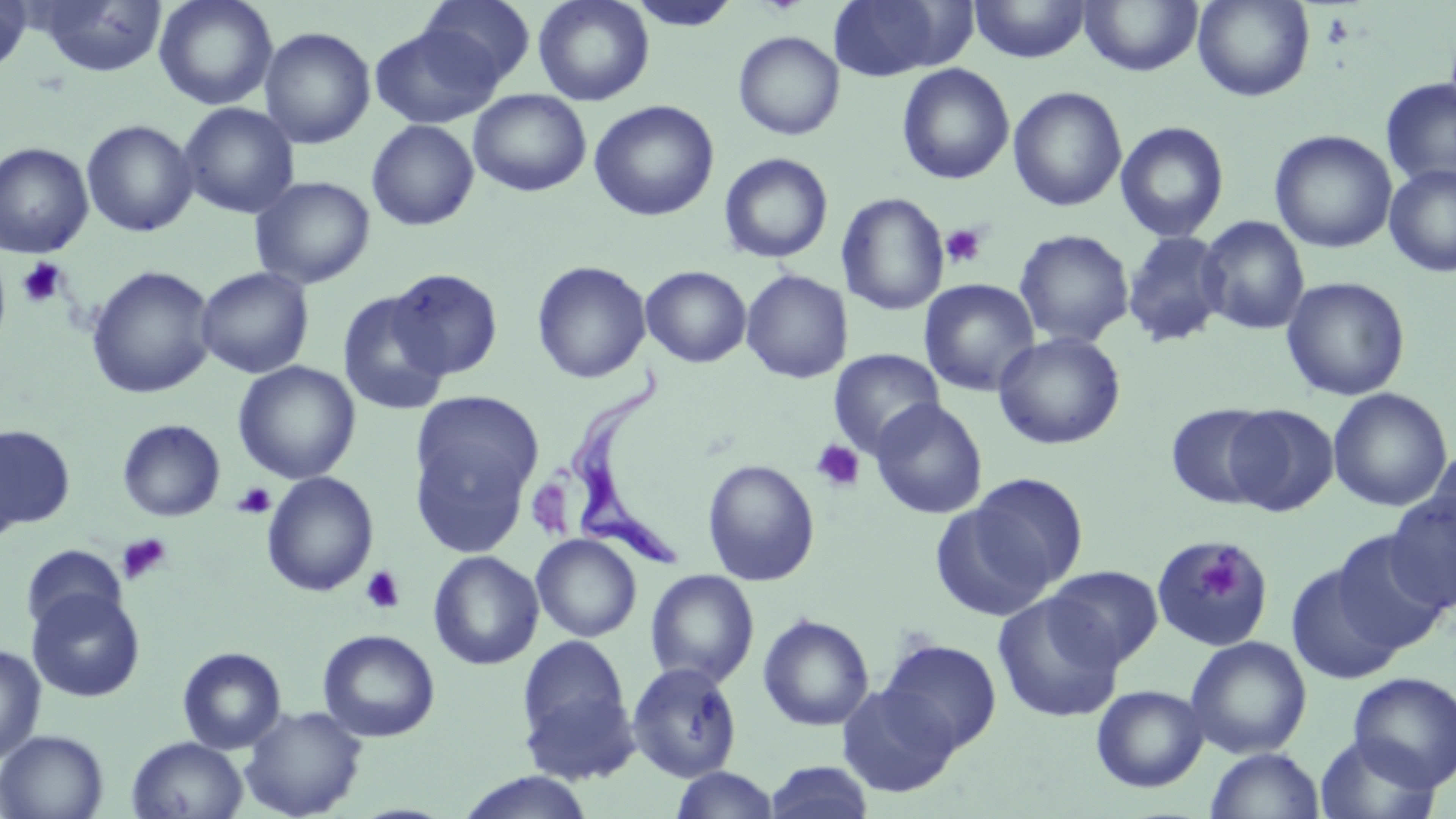

Approximate bounding boxes as [x1, y1, x2, y2] in pixels. Uninfected red blood cell locations: [0, 0, 33, 76], [37, 0, 167, 77], [154, 0, 278, 111], [418, 0, 536, 89], [533, 0, 655, 106], [626, 0, 742, 33], [825, 0, 968, 81], [970, 0, 1091, 63], [1078, 0, 1204, 76], [1192, 0, 1315, 102], [370, 24, 502, 129], [259, 26, 376, 149], [733, 31, 845, 140], [896, 62, 1015, 185], [1381, 77, 1456, 190], [1008, 86, 1127, 212], [468, 89, 591, 196], [588, 100, 719, 221], [177, 102, 300, 219], [81, 119, 198, 237], [366, 119, 480, 232], [1115, 120, 1230, 242], [1269, 130, 1397, 253], [0, 142, 94, 258], [718, 152, 834, 264], [1384, 164, 1456, 278], [249, 176, 375, 290], [837, 192, 949, 316], [1197, 215, 1310, 335], [1014, 228, 1135, 348], [1122, 230, 1230, 348], [531, 260, 651, 384], [86, 265, 217, 399], [641, 265, 752, 368], [195, 266, 315, 379], [389, 267, 503, 380], [740, 269, 853, 384], [1281, 276, 1411, 401], [919, 278, 1040, 396], [336, 291, 451, 416], [992, 331, 1126, 450], [828, 348, 945, 459], [233, 361, 361, 484], [1327, 388, 1453, 512], [411, 390, 544, 515], [869, 398, 989, 520], [1165, 403, 1276, 509], [1223, 404, 1339, 517], [117, 419, 225, 522], [1, 424, 76, 532], [1425, 442, 1456, 556], [701, 459, 820, 585], [262, 472, 379, 596], [960, 472, 1089, 599], [1386, 490, 1456, 613], [928, 498, 1061, 625], [1331, 530, 1452, 654], [531, 533, 642, 642], [1150, 539, 1274, 651], [21, 544, 128, 635], [428, 550, 544, 670], [1285, 563, 1405, 685], [1046, 565, 1165, 669], [644, 569, 760, 688], [26, 588, 145, 703], [992, 593, 1125, 723], [757, 612, 875, 731], [318, 629, 440, 742], [517, 634, 633, 755], [1185, 635, 1312, 759], [878, 638, 1002, 754], [0, 644, 47, 765], [177, 646, 286, 754], [626, 662, 743, 782], [1347, 672, 1456, 790], [519, 683, 641, 786], [836, 683, 961, 797], [1091, 684, 1209, 792], [239, 704, 368, 819], [0, 729, 108, 819], [1314, 733, 1442, 819], [127, 736, 248, 819], [1205, 747, 1325, 819], [763, 760, 876, 819], [669, 766, 781, 818], [456, 771, 596, 819]. Trypanosoma brucei locations: [567, 370, 686, 569]. Platelet locations: [940, 223, 989, 269], [17, 257, 68, 308], [810, 438, 865, 492], [233, 483, 276, 519], [118, 533, 172, 585], [1197, 550, 1242, 600], [360, 566, 406, 614]. Slide-level diagnosis: Trypanosoma brucei. One field of a larger specimen. Optical microscopy. Captured at 1000x magnification. May-Grünwald-Giemsa stain. Image is 1456×819 pixels. Thin blood smear.